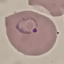
Result: malaria parasites detected. Thin smear of blood. Giemsa stain. Photographed with a smartphone camera at the microscope eyepiece. Automatically extracted cell patch, resized to 64 × 64 pixels.